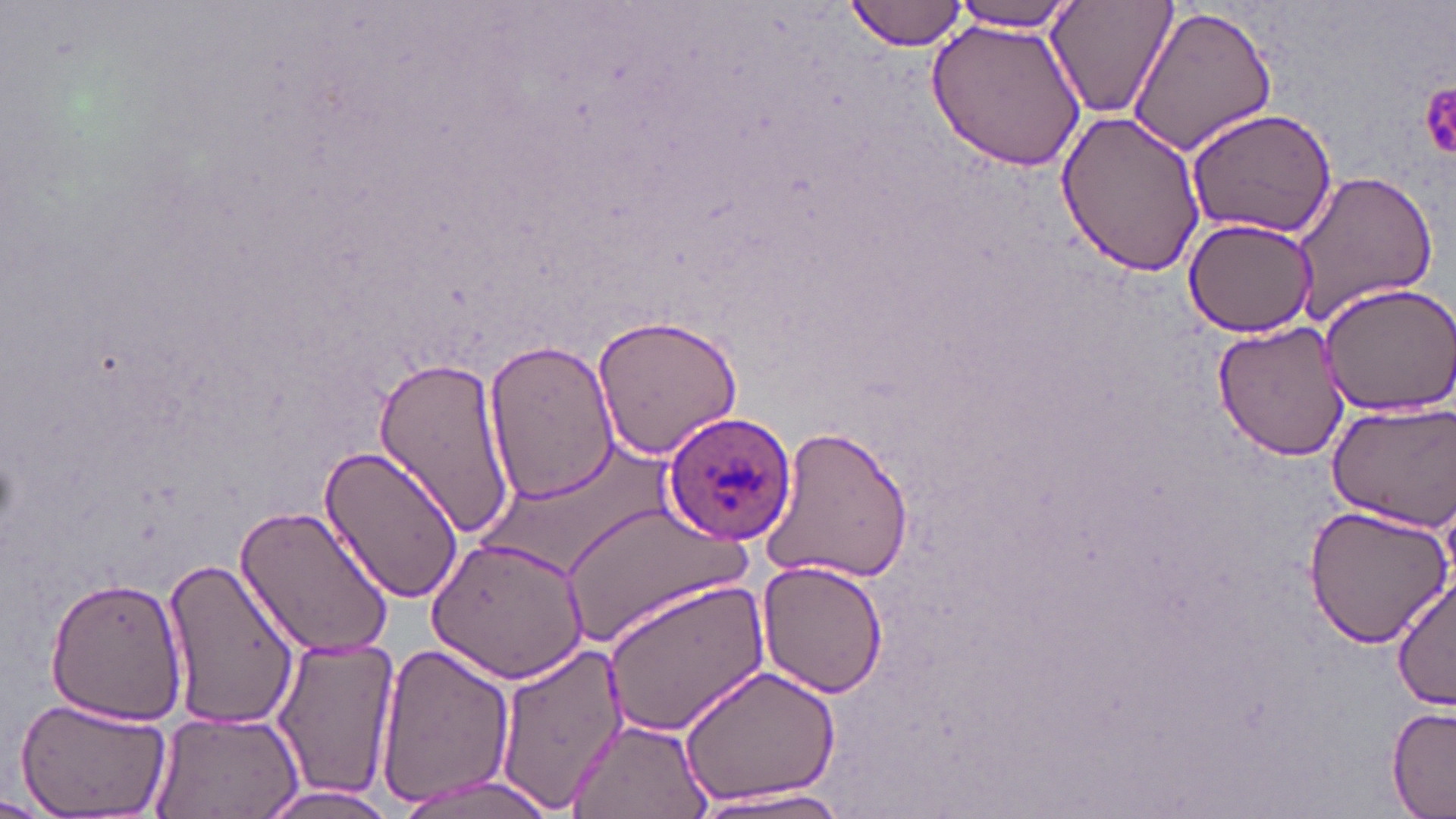
Approximate bounding boxes as [x1, y1, x2, y2] in pixels. Platelet locations: [1420, 79, 1456, 162]. Uninfected red blood cell locations: [846, 0, 971, 52], [1046, 0, 1178, 120], [944, 2, 1087, 31], [1127, 4, 1280, 158], [925, 14, 1090, 173], [1185, 107, 1337, 241], [1055, 111, 1208, 278], [1288, 167, 1439, 324], [1181, 215, 1320, 336], [1316, 281, 1456, 416], [590, 311, 745, 461], [1212, 317, 1354, 459], [483, 336, 619, 503], [370, 353, 518, 541], [1325, 399, 1456, 532], [756, 424, 916, 586], [317, 443, 464, 607], [235, 502, 396, 662], [563, 503, 746, 650], [1300, 503, 1452, 647], [427, 535, 591, 685], [161, 553, 303, 734], [757, 558, 887, 700], [47, 575, 191, 726], [1391, 576, 1456, 710], [600, 577, 768, 739], [268, 639, 400, 803], [489, 642, 627, 813], [374, 643, 513, 808], [676, 661, 847, 811], [14, 695, 176, 817], [1385, 705, 1455, 816], [149, 710, 303, 818], [566, 716, 715, 819], [389, 775, 563, 818], [250, 784, 403, 818], [688, 786, 860, 816]. Plasmodium ovale-infected red blood cell locations: [661, 411, 797, 544]. Slide-level diagnosis: Plasmodium ovale. May-Grünwald-Giemsa stain. One field of a larger specimen. Thin blood film. 1000x magnification. Optical microscopy. Image is 1456×819 pixels.